State the preparation type.
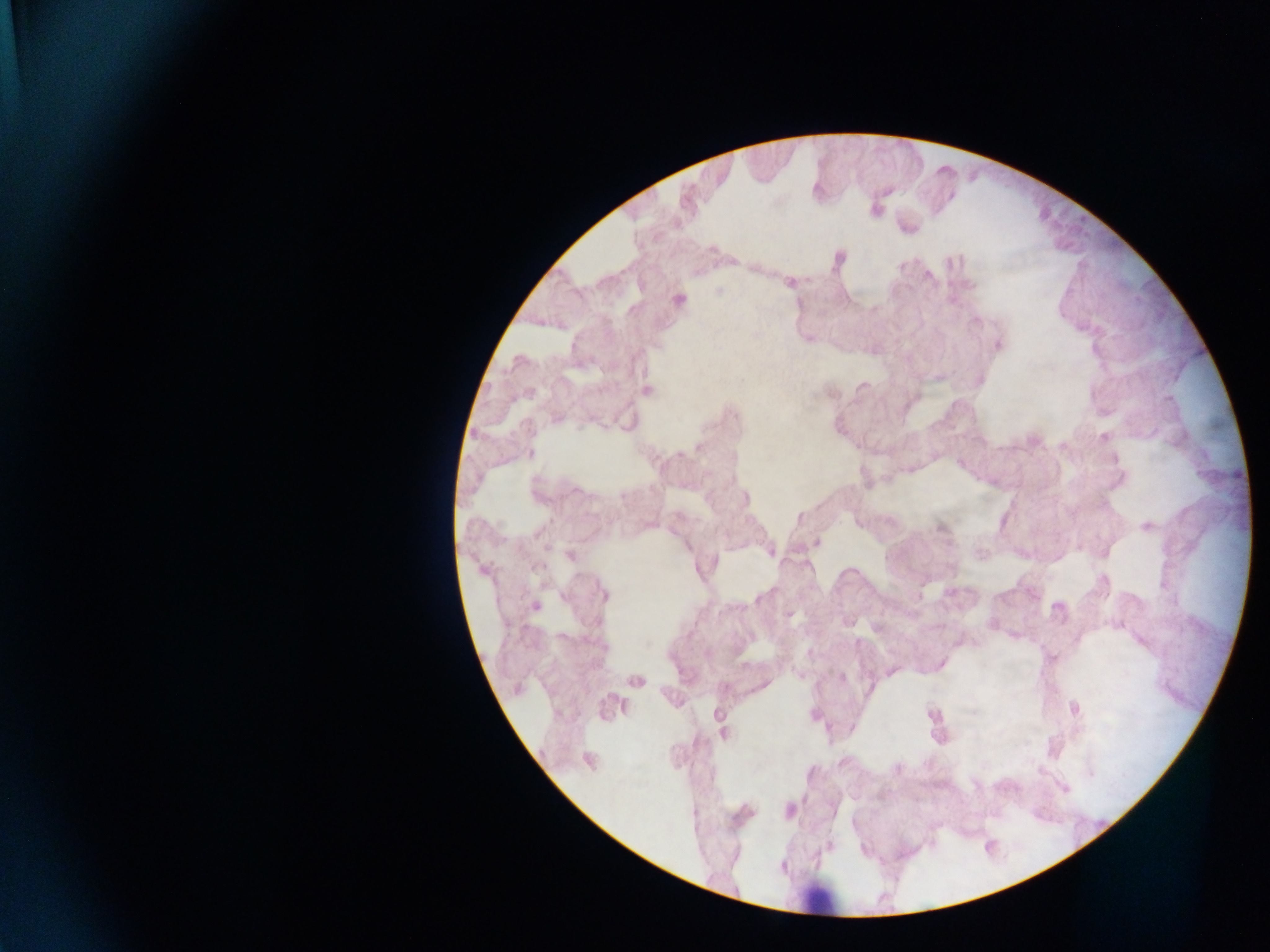
This is a thick smear.

field_of_view: single
image_size: 1270×952 pixels
leukocyte_locations: 'approximate centers as [x, y] in pixels: [818, 898]'
country: Ghana
capture: mobile-phone photograph through a microscope